Locate every blood parasite and identify its species.
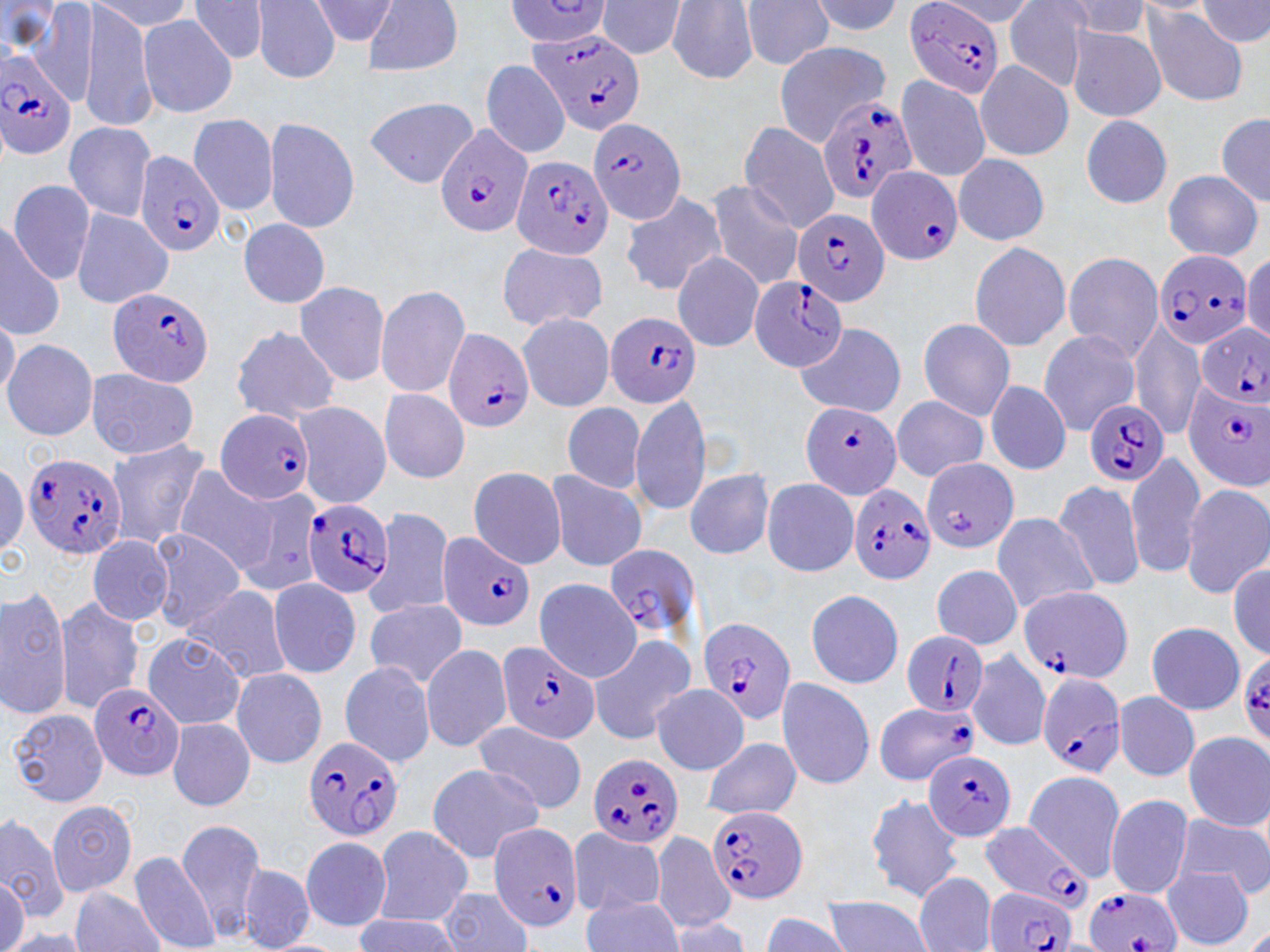
Approximate bounding boxes as named x1/y1/x2/y2 corners in pixels.
Plasmodium falciparum-infected red blood cells: (x1=901, y1=1, x2=1008, y2=97), (x1=524, y1=31, x2=647, y2=136), (x1=1, y1=49, x2=78, y2=158), (x1=815, y1=96, x2=916, y2=207), (x1=587, y1=117, x2=690, y2=222), (x1=434, y1=129, x2=531, y2=237), (x1=121, y1=145, x2=226, y2=259), (x1=513, y1=155, x2=613, y2=258), (x1=865, y1=163, x2=962, y2=264), (x1=794, y1=211, x2=889, y2=309), (x1=1157, y1=252, x2=1253, y2=348), (x1=748, y1=276, x2=848, y2=375), (x1=106, y1=287, x2=211, y2=385), (x1=605, y1=308, x2=700, y2=407), (x1=1193, y1=321, x2=1269, y2=408), (x1=444, y1=326, x2=537, y2=429), (x1=1176, y1=379, x2=1269, y2=492), (x1=799, y1=398, x2=902, y2=493), (x1=1082, y1=401, x2=1170, y2=485), (x1=219, y1=411, x2=310, y2=507), (x1=23, y1=453, x2=130, y2=558), (x1=850, y1=483, x2=940, y2=579), (x1=303, y1=500, x2=398, y2=598), (x1=438, y1=534, x2=530, y2=631), (x1=1018, y1=588, x2=1130, y2=685), (x1=697, y1=616, x2=792, y2=732), (x1=899, y1=630, x2=992, y2=721), (x1=499, y1=644, x2=599, y2=745), (x1=1039, y1=673, x2=1125, y2=779), (x1=89, y1=680, x2=180, y2=783), (x1=870, y1=702, x2=987, y2=785), (x1=302, y1=738, x2=402, y2=839), (x1=925, y1=751, x2=1014, y2=841), (x1=587, y1=752, x2=684, y2=846), (x1=707, y1=806, x2=808, y2=902), (x1=980, y1=822, x2=1104, y2=910), (x1=489, y1=823, x2=579, y2=934), (x1=977, y1=887, x2=1077, y2=952), (x1=1081, y1=890, x2=1181, y2=952).
No Plasmodium ovale, Plasmodium malariae, Plasmodium vivax, Babesia divergens, or Trypanosoma brucei observed.

Uninfected red blood cell locations: (x1=40, y1=0, x2=95, y2=107), (x1=76, y1=0, x2=159, y2=129), (x1=190, y1=0, x2=268, y2=63), (x1=244, y1=0, x2=337, y2=79), (x1=365, y1=0, x2=459, y2=74), (x1=502, y1=0, x2=608, y2=47), (x1=653, y1=0, x2=759, y2=79), (x1=733, y1=0, x2=835, y2=65), (x1=814, y1=0, x2=905, y2=38), (x1=595, y1=1, x2=684, y2=57), (x1=1003, y1=2, x2=1092, y2=88), (x1=1137, y1=3, x2=1253, y2=98), (x1=136, y1=12, x2=237, y2=120), (x1=1061, y1=19, x2=1166, y2=125), (x1=773, y1=42, x2=896, y2=113), (x1=479, y1=60, x2=567, y2=161), (x1=978, y1=61, x2=1073, y2=161), (x1=893, y1=71, x2=990, y2=183), (x1=366, y1=94, x2=479, y2=179), (x1=1079, y1=109, x2=1169, y2=210), (x1=186, y1=113, x2=286, y2=210), (x1=1216, y1=113, x2=1270, y2=204), (x1=264, y1=120, x2=361, y2=232), (x1=736, y1=121, x2=841, y2=238), (x1=58, y1=122, x2=162, y2=226), (x1=954, y1=153, x2=1049, y2=246), (x1=1162, y1=165, x2=1258, y2=261), (x1=6, y1=180, x2=102, y2=289), (x1=702, y1=181, x2=809, y2=289), (x1=618, y1=195, x2=728, y2=293), (x1=69, y1=203, x2=170, y2=315), (x1=233, y1=215, x2=324, y2=310), (x1=0, y1=218, x2=68, y2=340), (x1=969, y1=239, x2=1079, y2=354), (x1=492, y1=240, x2=610, y2=328), (x1=668, y1=246, x2=764, y2=347), (x1=1064, y1=253, x2=1163, y2=365), (x1=291, y1=280, x2=386, y2=386), (x1=368, y1=285, x2=474, y2=397), (x1=513, y1=307, x2=611, y2=415), (x1=916, y1=314, x2=1015, y2=422), (x1=1130, y1=322, x2=1203, y2=435), (x1=790, y1=327, x2=907, y2=419), (x1=1040, y1=327, x2=1123, y2=434), (x1=228, y1=328, x2=336, y2=429), (x1=8, y1=340, x2=98, y2=441), (x1=89, y1=368, x2=196, y2=454), (x1=983, y1=378, x2=1071, y2=476), (x1=380, y1=388, x2=468, y2=482), (x1=628, y1=397, x2=717, y2=516), (x1=890, y1=397, x2=990, y2=488), (x1=561, y1=398, x2=650, y2=495), (x1=300, y1=403, x2=394, y2=509), (x1=105, y1=438, x2=211, y2=549), (x1=923, y1=452, x2=1014, y2=551), (x1=171, y1=464, x2=277, y2=573), (x1=546, y1=467, x2=650, y2=569), (x1=685, y1=468, x2=772, y2=563), (x1=462, y1=469, x2=567, y2=565), (x1=1126, y1=474, x2=1208, y2=574), (x1=762, y1=475, x2=857, y2=575), (x1=1054, y1=481, x2=1147, y2=586), (x1=1180, y1=484, x2=1269, y2=596), (x1=244, y1=489, x2=315, y2=596), (x1=381, y1=510, x2=450, y2=612), (x1=992, y1=513, x2=1101, y2=611), (x1=150, y1=527, x2=248, y2=633), (x1=89, y1=534, x2=176, y2=629), (x1=604, y1=547, x2=698, y2=632), (x1=927, y1=556, x2=1019, y2=651), (x1=536, y1=578, x2=646, y2=680), (x1=267, y1=579, x2=362, y2=678), (x1=799, y1=583, x2=900, y2=688), (x1=178, y1=586, x2=299, y2=685), (x1=0, y1=591, x2=69, y2=723), (x1=56, y1=596, x2=139, y2=709), (x1=364, y1=600, x2=463, y2=685), (x1=1146, y1=618, x2=1240, y2=715), (x1=141, y1=630, x2=245, y2=732), (x1=590, y1=632, x2=696, y2=742), (x1=420, y1=646, x2=512, y2=754), (x1=969, y1=651, x2=1047, y2=751), (x1=337, y1=662, x2=437, y2=761), (x1=232, y1=664, x2=322, y2=765), (x1=771, y1=677, x2=878, y2=789), (x1=1113, y1=685, x2=1197, y2=783), (x1=650, y1=693, x2=750, y2=778), (x1=7, y1=705, x2=108, y2=802), (x1=168, y1=718, x2=261, y2=809), (x1=473, y1=724, x2=588, y2=814), (x1=1181, y1=731, x2=1270, y2=831), (x1=695, y1=738, x2=803, y2=818), (x1=424, y1=766, x2=544, y2=867), (x1=1025, y1=771, x2=1120, y2=877), (x1=865, y1=793, x2=968, y2=906), (x1=1100, y1=798, x2=1191, y2=898), (x1=47, y1=800, x2=137, y2=894), (x1=0, y1=813, x2=69, y2=927), (x1=1174, y1=814, x2=1270, y2=895), (x1=175, y1=821, x2=263, y2=941), (x1=374, y1=828, x2=471, y2=925), (x1=567, y1=829, x2=669, y2=911), (x1=650, y1=829, x2=729, y2=928), (x1=301, y1=834, x2=387, y2=933), (x1=126, y1=847, x2=218, y2=948), (x1=237, y1=859, x2=311, y2=951), (x1=1159, y1=866, x2=1252, y2=948), (x1=910, y1=876, x2=998, y2=951), (x1=578, y1=880, x2=684, y2=952), (x1=69, y1=886, x2=161, y2=952), (x1=436, y1=889, x2=529, y2=952), (x1=818, y1=893, x2=928, y2=952). Slide-level diagnosis: Plasmodium falciparum. 1000x magnification. Image is 1270×952 pixels. Thin blood film. Optical microscopy. May-Grünwald-Giemsa stain. One field of a larger specimen.